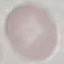

Summary:
  - Result: negative for malaria parasites
  - Stain: Giemsa
  - Image type: automatically extracted cell patch, resized to 64 × 64 pixels
  - Preparation: thin smear
  - Capture: smartphone through the microscope eyepiece